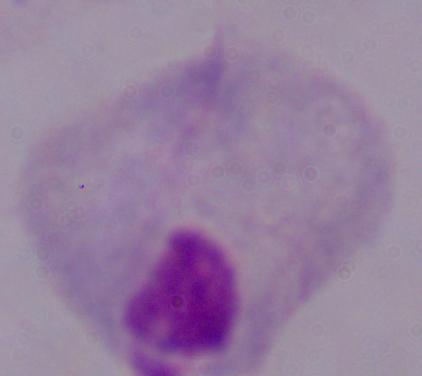
Micrograph. A trichomonad is shown. 1000x magnification.